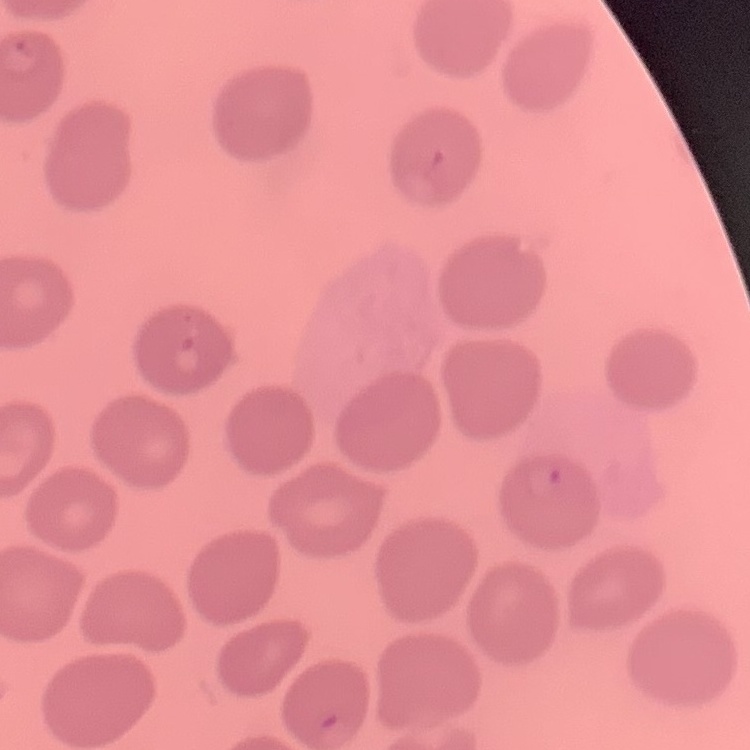
Summary:
  - Red blood cell morphology: no rouleaux formation
  - Image type: square crop of a larger photomicrograph
  - Stain: Field's or Giemsa
  - Preparation: thin blood film